Outline each blood parasite and name the species.
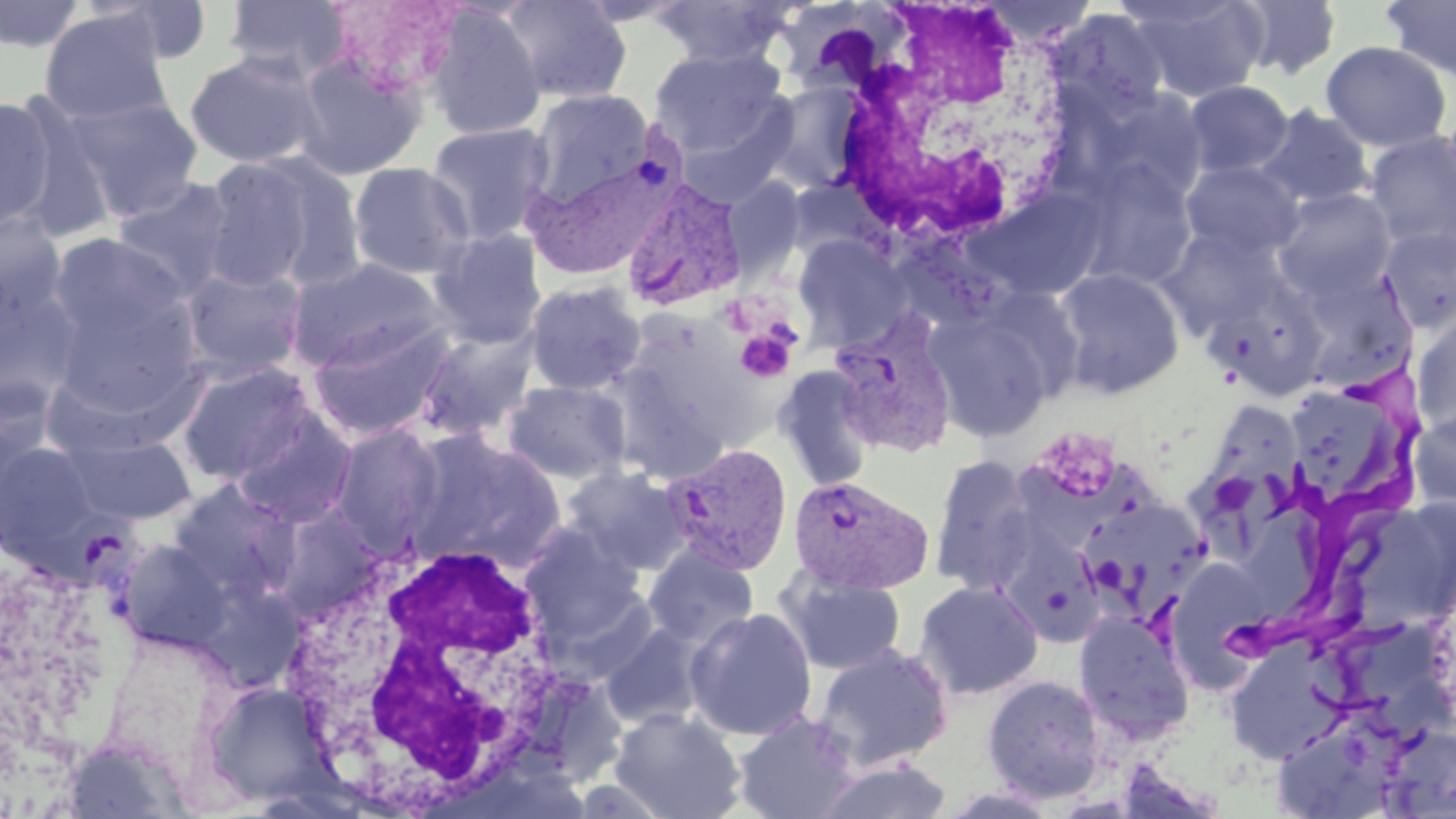
Approximate bounding boxes as named x1/y1/x2/y2 corners in pixels.
Plasmodium vivax-infected red blood cells: (x1=527, y1=131, x2=689, y2=283), (x1=622, y1=177, x2=748, y2=312), (x1=826, y1=306, x2=959, y2=460), (x1=659, y1=442, x2=794, y2=577), (x1=788, y1=474, x2=935, y2=595).
No Plasmodium falciparum, Plasmodium ovale, Plasmodium malariae, Babesia divergens, or Trypanosoma brucei observed.

slide-level diagnosis = Plasmodium vivax
white blood cell locations = approximate bounding boxes as named x1/y1/x2/y2 corners in pixels: (x1=810, y1=4, x2=1080, y2=256), (x1=284, y1=529, x2=578, y2=815)
stain = May-Grünwald-Giemsa
magnification = 1000x
platelet locations = approximate bounding boxes as named x1/y1/x2/y2 corners in pixels: (x1=733, y1=326, x2=799, y2=383)
image size = 1456×819 pixels
field of view = single
modality = light microscopy
preparation = thin blood film
uninfected red blood cell locations = approximate bounding boxes as named x1/y1/x2/y2 corners in pixels: (x1=222, y1=0, x2=352, y2=84), (x1=498, y1=0, x2=633, y2=104), (x1=1230, y1=0, x2=1343, y2=81), (x1=1381, y1=0, x2=1456, y2=84), (x1=0, y1=1, x2=85, y2=54), (x1=1123, y1=1, x2=1271, y2=102), (x1=648, y1=2, x2=792, y2=67), (x1=426, y1=5, x2=546, y2=141), (x1=39, y1=10, x2=173, y2=126), (x1=1054, y1=10, x2=1173, y2=116), (x1=1320, y1=41, x2=1452, y2=153), (x1=650, y1=47, x2=787, y2=158), (x1=184, y1=51, x2=324, y2=169), (x1=293, y1=51, x2=427, y2=180), (x1=1182, y1=80, x2=1294, y2=179), (x1=761, y1=83, x2=868, y2=195), (x1=1089, y1=87, x2=1208, y2=209), (x1=529, y1=89, x2=655, y2=207), (x1=65, y1=95, x2=204, y2=221), (x1=0, y1=97, x2=58, y2=229), (x1=10, y1=98, x2=117, y2=240), (x1=1255, y1=105, x2=1375, y2=210), (x1=426, y1=122, x2=555, y2=245), (x1=1363, y1=131, x2=1456, y2=254), (x1=199, y1=153, x2=360, y2=293), (x1=1071, y1=160, x2=1200, y2=290), (x1=1181, y1=160, x2=1304, y2=262), (x1=348, y1=162, x2=474, y2=280), (x1=723, y1=177, x2=809, y2=280), (x1=112, y1=179, x2=235, y2=298), (x1=1272, y1=188, x2=1397, y2=303), (x1=965, y1=189, x2=1106, y2=302), (x1=0, y1=215, x2=67, y2=334), (x1=1379, y1=226, x2=1456, y2=335), (x1=1156, y1=227, x2=1290, y2=342), (x1=429, y1=229, x2=547, y2=349), (x1=49, y1=233, x2=186, y2=346), (x1=792, y1=234, x2=912, y2=352), (x1=287, y1=257, x2=446, y2=372), (x1=1286, y1=261, x2=1419, y2=394), (x1=180, y1=267, x2=308, y2=381), (x1=1052, y1=267, x2=1185, y2=399), (x1=1201, y1=270, x2=1330, y2=401), (x1=524, y1=281, x2=646, y2=396), (x1=52, y1=289, x2=204, y2=425), (x1=928, y1=306, x2=1054, y2=442), (x1=1411, y1=314, x2=1456, y2=439), (x1=618, y1=315, x2=761, y2=462), (x1=309, y1=321, x2=452, y2=441), (x1=415, y1=323, x2=540, y2=441), (x1=177, y1=362, x2=317, y2=485), (x1=773, y1=365, x2=877, y2=490), (x1=502, y1=379, x2=631, y2=484), (x1=1203, y1=401, x2=1298, y2=558), (x1=1409, y1=407, x2=1456, y2=517), (x1=231, y1=409, x2=358, y2=527), (x1=330, y1=425, x2=445, y2=550), (x1=403, y1=429, x2=565, y2=572), (x1=65, y1=435, x2=197, y2=524), (x1=1, y1=443, x2=103, y2=570), (x1=929, y1=454, x2=1039, y2=596), (x1=1023, y1=454, x2=1157, y2=556), (x1=564, y1=467, x2=690, y2=576), (x1=169, y1=480, x2=299, y2=601), (x1=1076, y1=495, x2=1210, y2=619), (x1=271, y1=508, x2=380, y2=618), (x1=1345, y1=514, x2=1449, y2=628), (x1=517, y1=524, x2=646, y2=651), (x1=997, y1=532, x2=1106, y2=648), (x1=118, y1=540, x2=233, y2=652), (x1=643, y1=546, x2=759, y2=648), (x1=1182, y1=561, x2=1270, y2=694), (x1=782, y1=570, x2=906, y2=675), (x1=913, y1=580, x2=1044, y2=700), (x1=685, y1=607, x2=817, y2=741), (x1=1074, y1=609, x2=1195, y2=743), (x1=598, y1=622, x2=711, y2=730), (x1=1231, y1=636, x2=1355, y2=767), (x1=813, y1=643, x2=954, y2=771), (x1=982, y1=674, x2=1107, y2=804), (x1=201, y1=679, x2=326, y2=806), (x1=610, y1=708, x2=746, y2=819), (x1=731, y1=711, x2=861, y2=819), (x1=1386, y1=727, x2=1456, y2=819), (x1=1279, y1=729, x2=1400, y2=819), (x1=812, y1=758, x2=955, y2=818), (x1=934, y1=787, x2=1063, y2=818)